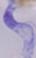
magnification = 1000x
modality = micrograph
identification = trypanosome